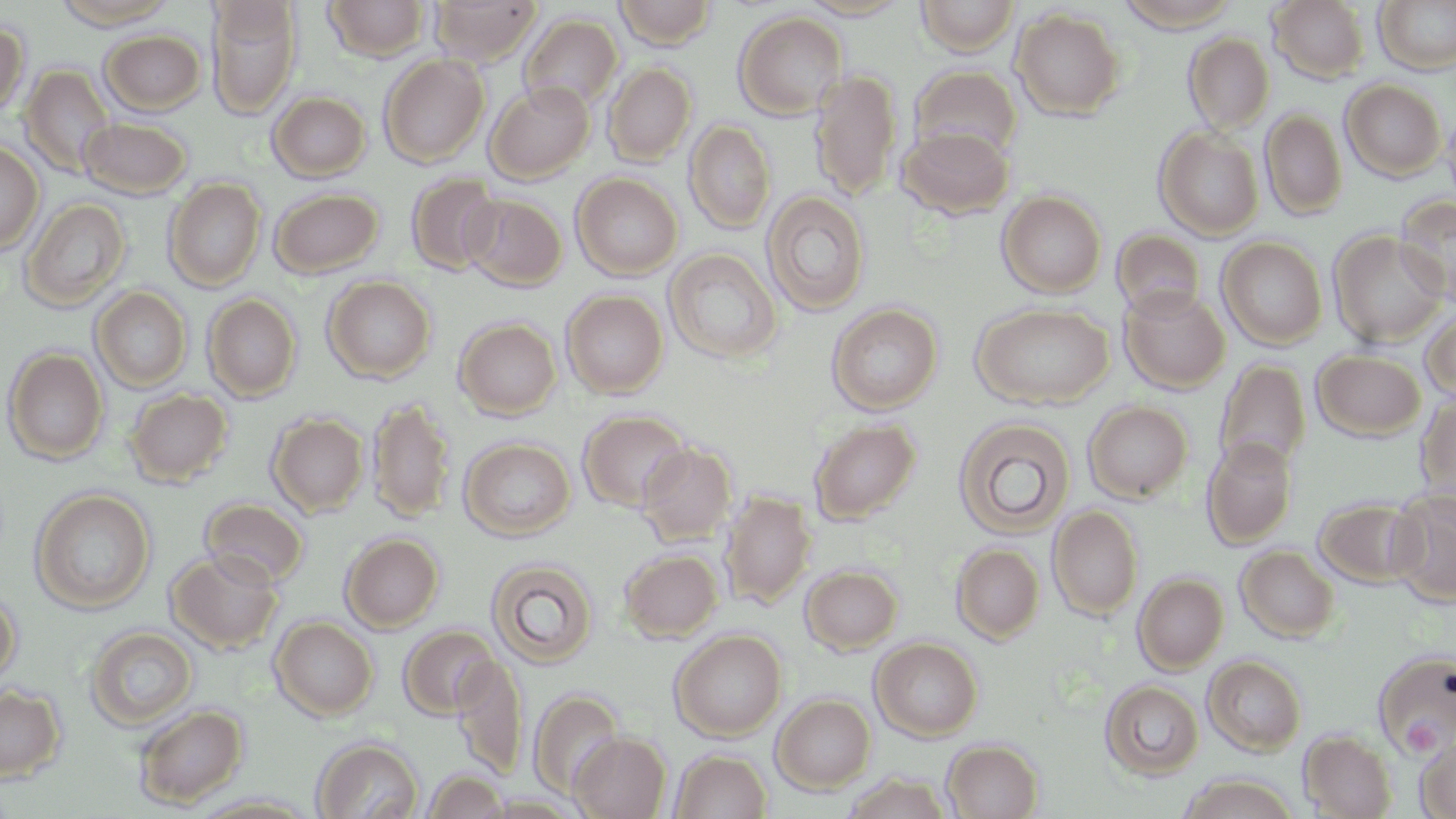

Summary:
  - Coordinate format: approximate bounding boxes as (x1, y1, x2, y2) in pixels
  - Platelet locations: (1402, 716, 1441, 754)
  - Uninfected red blood cell locations: (51, 0, 179, 30), (323, 0, 431, 60), (430, 0, 541, 65), (613, 0, 719, 49), (795, 0, 914, 20), (916, 0, 1020, 55), (1115, 0, 1243, 32), (205, 1, 301, 118), (1269, 1, 1370, 83), (1373, 1, 1456, 74), (1011, 9, 1125, 121), (733, 10, 848, 120), (519, 14, 623, 112), (0, 22, 29, 120), (100, 29, 206, 115), (1184, 32, 1274, 133), (379, 54, 489, 168), (603, 62, 696, 166), (20, 64, 116, 180), (909, 66, 1023, 164), (810, 68, 902, 201), (1340, 79, 1447, 181), (484, 81, 595, 184), (268, 92, 370, 182), (1441, 107, 1456, 212), (1260, 109, 1347, 220), (79, 116, 191, 199), (684, 120, 776, 235), (898, 124, 1015, 219), (1154, 126, 1264, 240), (0, 138, 44, 255), (406, 173, 503, 275), (572, 173, 683, 280), (164, 177, 266, 291), (269, 187, 384, 278), (762, 190, 870, 316), (997, 190, 1107, 298), (463, 194, 567, 290), (1394, 195, 1456, 306), (20, 197, 131, 311), (1111, 228, 1205, 318), (1328, 230, 1449, 347), (1217, 236, 1327, 349), (664, 248, 782, 364), (322, 276, 436, 383), (1119, 285, 1230, 393), (90, 287, 193, 392), (562, 290, 668, 398), (203, 293, 301, 402), (827, 302, 943, 414), (972, 303, 1114, 409), (1420, 308, 1456, 407), (454, 317, 561, 419), (2, 347, 109, 465), (1311, 350, 1426, 440), (1214, 357, 1310, 476), (125, 388, 233, 487), (1415, 390, 1456, 510), (367, 396, 455, 524), (1083, 400, 1194, 503), (577, 409, 692, 512), (267, 411, 369, 517), (953, 417, 1076, 539), (809, 418, 921, 524), (1202, 436, 1297, 549), (460, 437, 576, 541), (637, 442, 736, 545), (30, 488, 156, 614), (1387, 488, 1456, 606), (721, 490, 816, 608), (1313, 497, 1422, 587), (200, 498, 309, 588), (1048, 505, 1143, 620), (340, 532, 444, 632), (952, 543, 1045, 643), (1236, 545, 1340, 643), (619, 549, 722, 641), (167, 550, 284, 654), (486, 557, 599, 668), (800, 565, 903, 654), (1133, 572, 1228, 674), (0, 588, 21, 687), (270, 617, 378, 721), (85, 625, 198, 730), (399, 625, 499, 719), (670, 629, 787, 740), (871, 637, 983, 741), (1372, 649, 1456, 758), (451, 654, 528, 778), (1202, 654, 1307, 756), (1100, 680, 1204, 780), (0, 684, 65, 783), (529, 689, 624, 798), (771, 693, 876, 793), (133, 704, 248, 809), (1299, 729, 1397, 819), (1415, 729, 1456, 818), (568, 731, 671, 818), (312, 737, 423, 819), (941, 739, 1043, 819), (668, 749, 772, 818), (422, 770, 510, 818), (841, 772, 958, 818), (1177, 774, 1300, 818), (189, 794, 321, 818), (481, 794, 588, 817)
  - Slide-level diagnosis: no evidence of blood parasites
  - Field of view: one of a larger specimen
  - Image size: 1456×819 pixels
  - Modality: optical microscopy
  - Magnification: 1000x
  - Stain: May-Grünwald-Giemsa
  - Preparation: thin blood film